State which parasite is depicted.
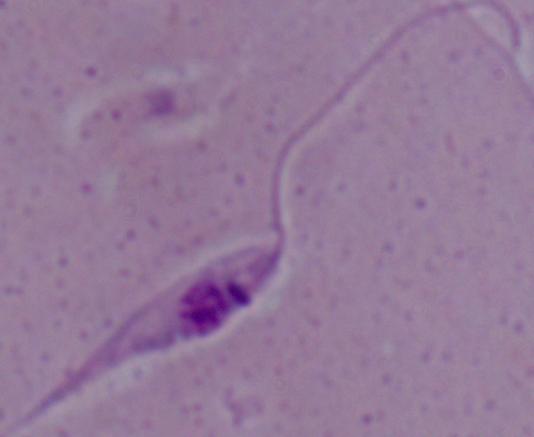

Leishmania.

Summary:
  - Magnification: 1000x
  - Modality: micrograph